Name the blood parasite species.
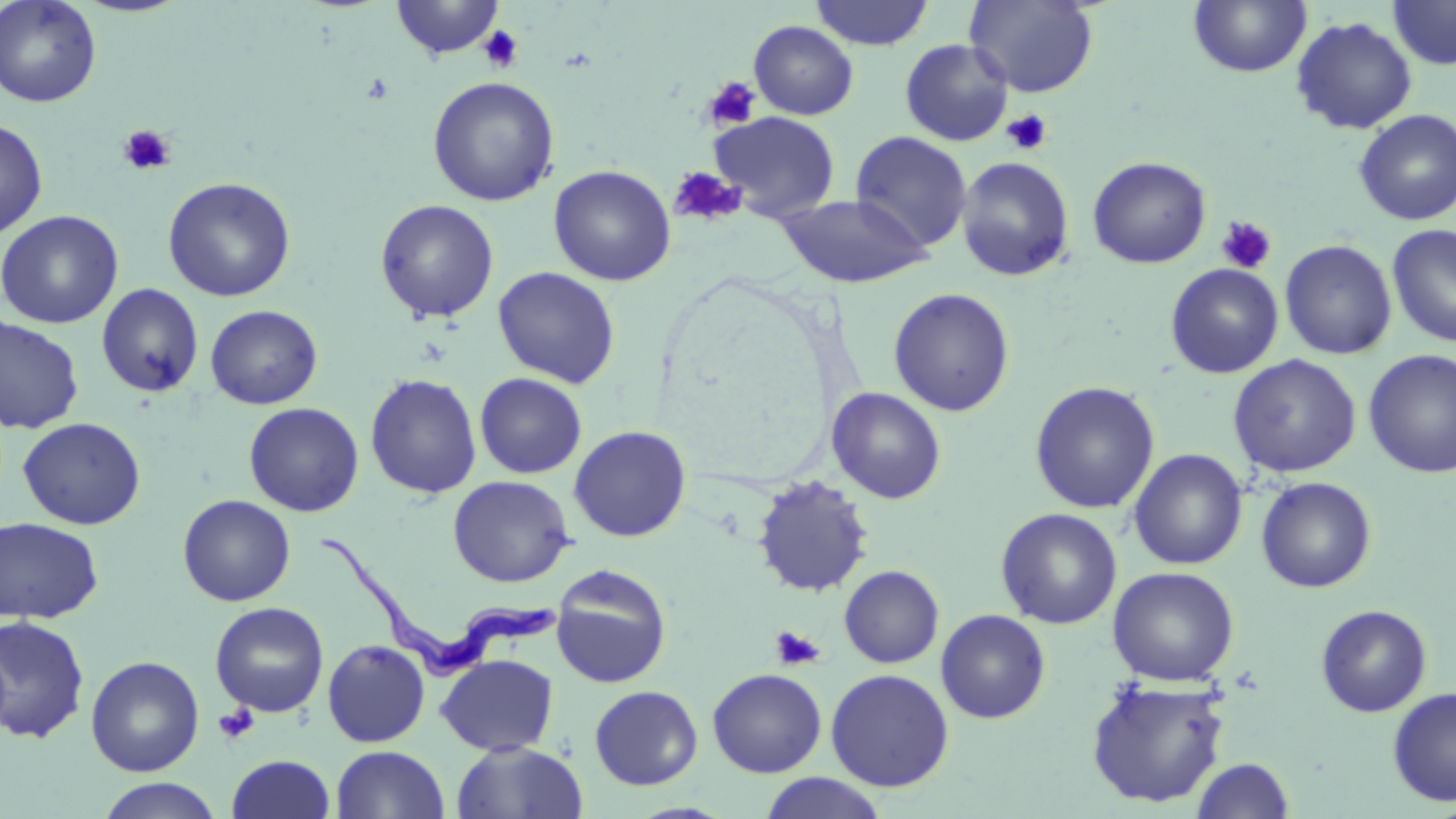

Trypanosoma brucei.

modality = optical microscopy
stain = May-Grünwald-Giemsa
magnification = 1000x
Trypanosoma brucei locations = approximate bounding boxes as (x1,y1)-(x2,y2) corner pairs in pixels: (319,536)-(559,685)
preparation = thin blood film
uninfected red blood cell locations = approximate bounding boxes as (x1,y1)-(x2,y2) corner pairs in pixels: (0,0)-(102,108), (390,0)-(505,59), (810,0)-(933,50), (965,0)-(1099,97), (1188,0)-(1312,78), (1388,1)-(1456,70), (1291,16)-(1417,134), (748,20)-(859,120), (899,39)-(1014,146), (427,76)-(560,206), (1354,110)-(1456,226), (709,111)-(840,220), (0,118)-(48,239), (849,131)-(972,253), (955,156)-(1075,282), (1087,156)-(1211,268), (549,165)-(676,286), (162,176)-(296,302), (775,193)-(932,289), (375,199)-(499,323), (0,210)-(123,329), (1387,223)-(1456,348), (1280,239)-(1397,360), (1165,263)-(1283,378), (493,266)-(621,388), (96,283)-(204,398), (888,287)-(1015,416), (205,304)-(323,409), (0,317)-(84,434), (1363,349)-(1456,478), (1227,354)-(1362,478), (474,372)-(587,479), (365,373)-(482,498), (1029,381)-(1160,514), (827,387)-(946,504), (244,402)-(364,517), (17,417)-(146,530), (569,425)-(691,542), (1129,448)-(1248,570), (448,475)-(575,587), (752,476)-(874,598), (1256,476)-(1377,593), (177,494)-(296,607), (996,507)-(1123,630), (0,517)-(103,624), (551,565)-(672,688), (839,565)-(943,668), (1107,566)-(1239,686), (210,602)-(329,717), (1316,604)-(1432,717), (936,609)-(1051,723), (0,616)-(91,744), (323,640)-(430,748), (436,654)-(559,756), (85,655)-(204,777), (707,668)-(827,777), (825,668)-(954,792), (1085,677)-(1231,808), (589,685)-(703,790), (1387,687)-(1456,806), (451,741)-(587,819), (331,745)-(449,819), (226,754)-(335,818), (1191,757)-(1294,818), (757,772)-(889,819), (95,778)-(224,819)
field of view = single
image size = 1456×819 pixels
platelet locations = approximate bounding boxes as (x1,y1)-(x2,y2) corner pairs in pixels: (478,25)-(524,73), (703,76)-(761,130), (1001,109)-(1053,155), (117,125)-(176,176), (670,166)-(745,227), (1216,216)-(1277,274), (770,625)-(825,670), (213,704)-(259,746)